Point out each Plasmodium parasite.
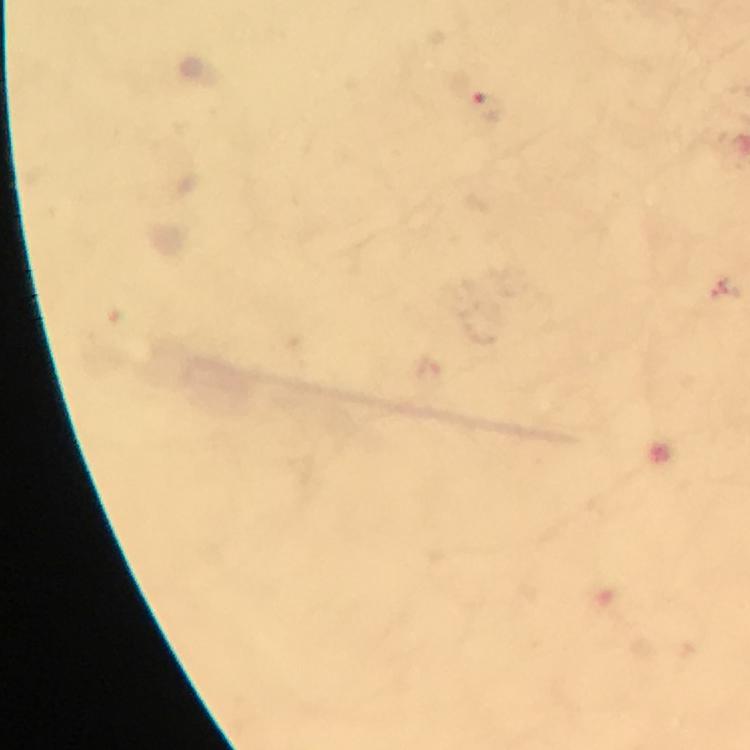
Approximate centers as {x, y} in pixels.
Plasmodium parasites: {486, 109}.

stain = Giemsa
magnification = 100x
capture = smartphone mounted on the microscope
image size = 750×750 pixels
context = from a malaria diagnostic workup
cropped from = a single field of view
preparation = thick blood smear
immersion oil = applied